Locate and identify every blood parasite.
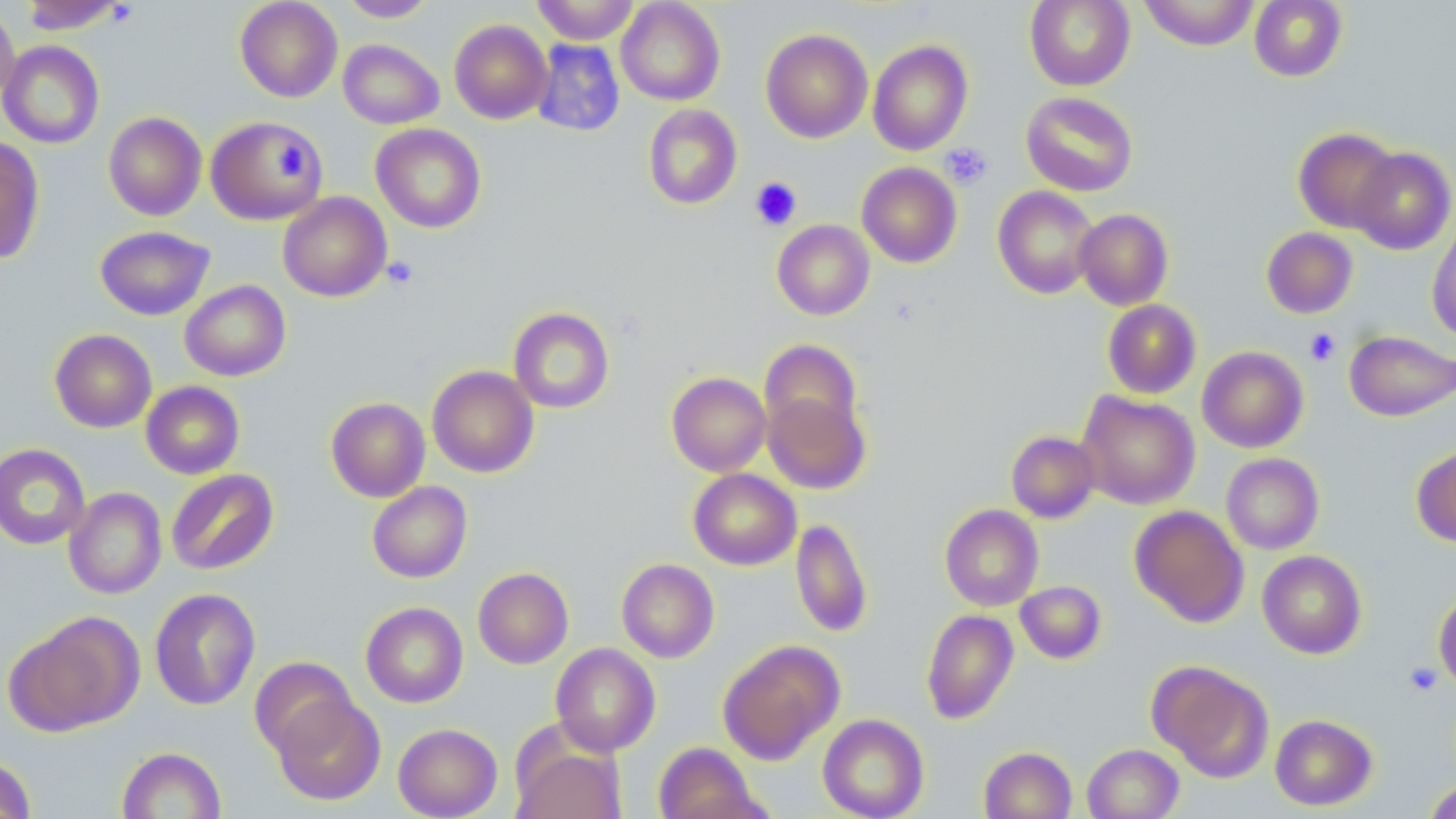

No blood parasites seen.

Summary:
  - Coordinate format: approximate bounding boxes as [x1, y1, x2, y2] in pixels
  - Uninfected red blood cell locations: [18, 0, 129, 34], [234, 0, 343, 103], [339, 0, 437, 22], [533, 0, 640, 44], [616, 0, 725, 106], [1024, 0, 1136, 90], [1138, 0, 1260, 50], [1249, 0, 1348, 82], [0, 3, 20, 108], [449, 19, 552, 124], [760, 28, 873, 143], [338, 39, 444, 129], [531, 39, 625, 137], [867, 39, 973, 155], [0, 40, 105, 149], [1021, 91, 1139, 196], [643, 104, 742, 209], [103, 112, 206, 221], [205, 116, 326, 225], [371, 124, 486, 233], [1293, 127, 1400, 233], [0, 136, 44, 264], [1349, 146, 1455, 255], [856, 162, 962, 268], [992, 185, 1100, 299], [278, 192, 391, 302], [1074, 208, 1173, 310], [1427, 216, 1456, 342], [772, 219, 874, 320], [95, 226, 215, 320], [1262, 227, 1358, 318], [179, 280, 291, 381], [1102, 299, 1202, 399], [508, 306, 614, 413], [49, 329, 157, 433], [1344, 330, 1456, 421], [759, 339, 863, 443], [1212, 345, 1314, 554], [1197, 346, 1308, 453], [427, 365, 539, 478], [666, 372, 772, 476], [140, 381, 245, 479], [1076, 390, 1200, 509], [763, 391, 870, 494], [326, 397, 430, 502], [1006, 431, 1099, 523], [0, 443, 90, 549], [1412, 444, 1456, 547], [1221, 453, 1324, 554], [688, 468, 801, 570], [166, 469, 279, 575], [367, 481, 472, 583], [64, 488, 167, 599], [939, 504, 1043, 611], [1129, 505, 1249, 627], [790, 517, 873, 638], [1257, 550, 1367, 659], [616, 558, 719, 663], [473, 567, 573, 669], [1015, 580, 1106, 664], [149, 587, 260, 711], [1433, 588, 1456, 691], [361, 602, 468, 707], [921, 609, 1018, 724], [6, 612, 142, 736], [717, 639, 844, 764], [550, 643, 660, 756], [249, 656, 357, 758], [1148, 661, 1274, 782], [271, 694, 385, 805], [818, 714, 929, 819], [1270, 714, 1377, 810], [393, 723, 502, 818], [512, 742, 626, 818], [654, 742, 766, 819], [1082, 743, 1184, 818], [979, 746, 1077, 819], [117, 747, 226, 819], [0, 755, 36, 818], [1423, 779, 1456, 819]
  - Platelet locations: [940, 142, 993, 189], [274, 144, 309, 180], [750, 176, 802, 230], [382, 255, 419, 290], [1305, 328, 1341, 366], [1403, 663, 1442, 695]
  - Slide-level diagnosis: no evidence of blood parasites
  - Magnification: 1000x
  - Modality: optical microscopy
  - Stain: May-Grünwald-Giemsa
  - Image size: 1456×819 pixels
  - Preparation: thin blood film
  - Field of view: one of a larger specimen